Outline each uninfected red blood cell.
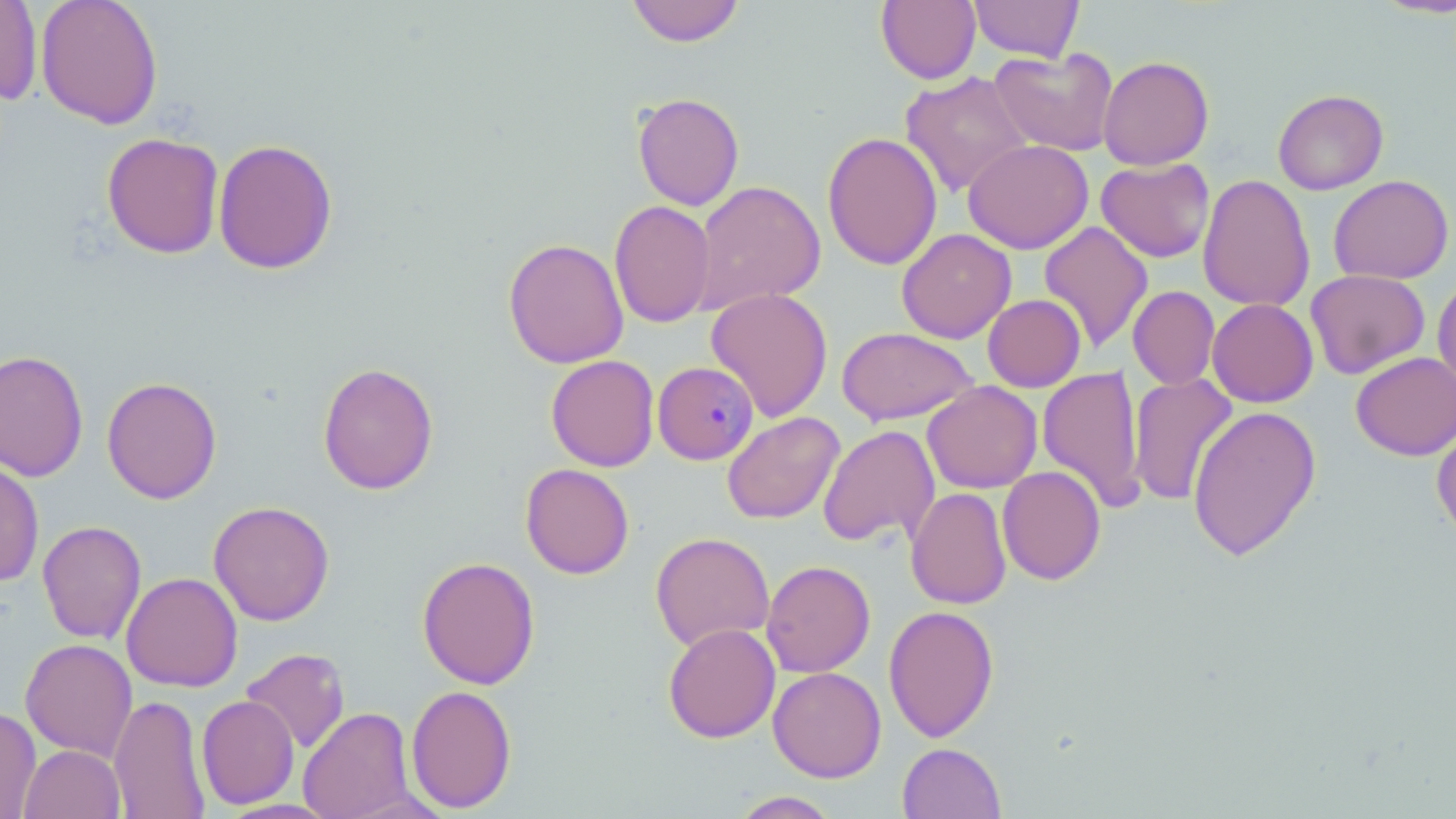
Approximate bounding boxes as [x1, y1, x2, y2] in pixels.
Uninfected red blood cells (subset): [0, 0, 43, 107], [36, 0, 163, 129], [627, 0, 745, 47], [876, 0, 981, 84], [968, 0, 1084, 62], [1371, 0, 1456, 19], [989, 47, 1118, 156], [1098, 55, 1214, 170], [900, 70, 1034, 198], [1272, 88, 1389, 195], [632, 92, 745, 211], [822, 131, 943, 271], [101, 132, 224, 259], [213, 138, 338, 275], [963, 139, 1094, 254], [1096, 158, 1215, 263], [1198, 174, 1315, 313], [1328, 174, 1454, 284], [691, 179, 827, 314], [609, 200, 715, 328], [1039, 221, 1154, 353], [897, 228, 1016, 343], [503, 238, 629, 369], [1305, 269, 1430, 379], [1433, 274, 1456, 398], [1128, 286, 1220, 390], [705, 288, 833, 422], [983, 294, 1085, 392], [1207, 298, 1319, 407], [836, 327, 978, 425], [0, 349, 89, 482], [1350, 352, 1456, 460], [546, 354, 659, 471], [317, 362, 439, 495], [1037, 366, 1146, 511], [1127, 373, 1238, 507], [101, 376, 222, 504], [922, 381, 1043, 493], [1187, 405, 1322, 561], [722, 412, 845, 524], [1431, 422, 1456, 543], [818, 424, 940, 549], [0, 460, 44, 587], [520, 463, 634, 579], [997, 466, 1105, 585], [905, 487, 1011, 609], [208, 500, 335, 626], [37, 520, 147, 644], [650, 532, 775, 652], [417, 556, 541, 689], [761, 560, 875, 677], [121, 572, 243, 692], [883, 605, 999, 742], [663, 623, 781, 743], [20, 638, 138, 762], [240, 647, 350, 754], [768, 666, 886, 782], [406, 684, 517, 813], [109, 694, 211, 819], [197, 695, 299, 809], [298, 706, 416, 819], [0, 707, 42, 818], [897, 742, 1006, 819], [19, 744, 125, 819], [729, 791, 841, 818].

Summary:
  - Slide-level diagnosis: Plasmodium malariae
  - Field of view: single
  - Stain: May-Grünwald-Giemsa
  - Image size: 1456×819 pixels
  - Preparation: thin blood film
  - Modality: light microscopy
  - Magnification: 1000x